Assess this cell for malaria.
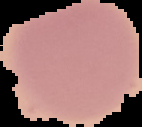
It is uninfected.

image size = 142×127 pixels
preparation = thin blood film
image type = segmented cell region on a black background